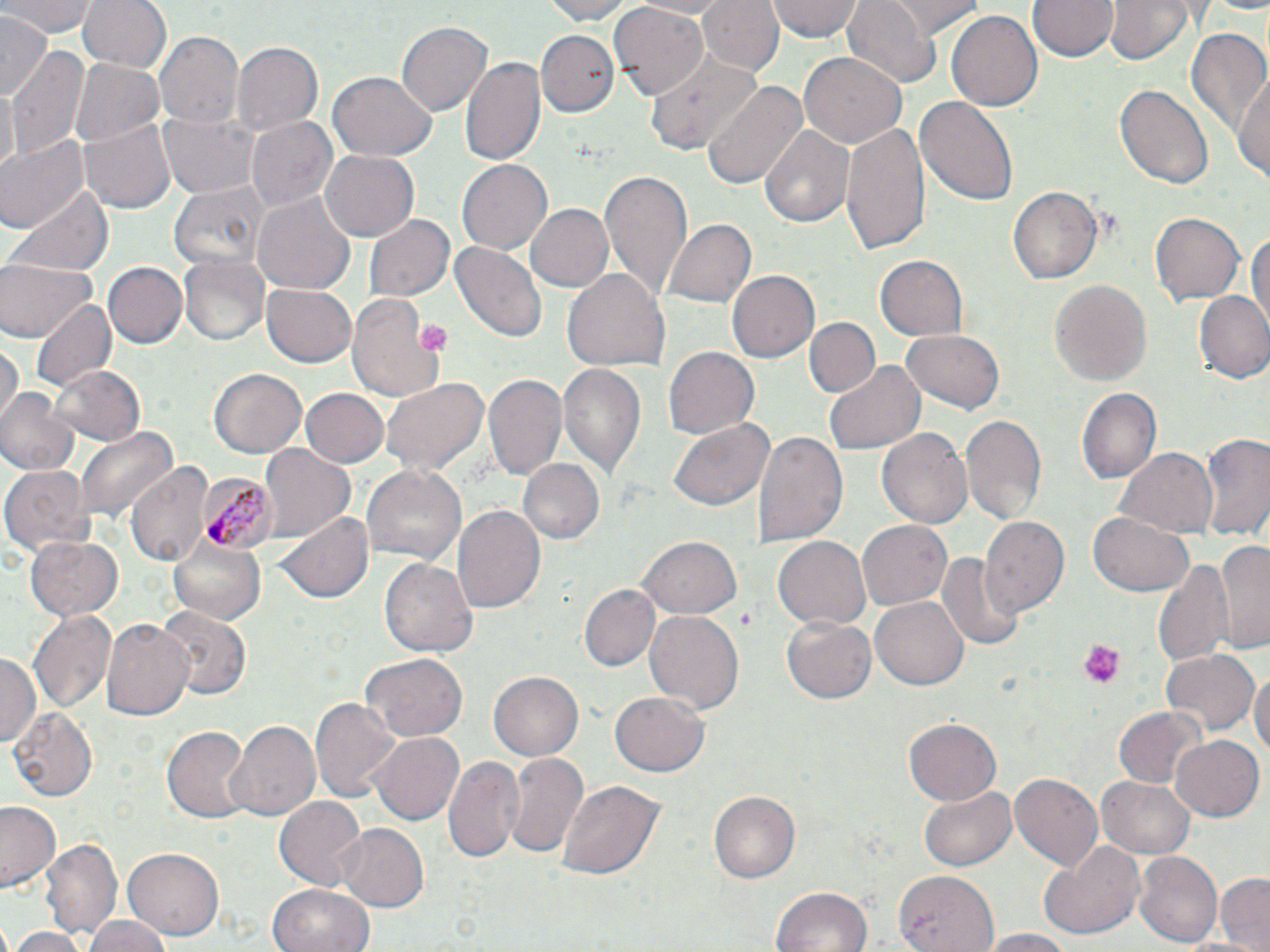 Approximate bounding boxes as [x1, y1, x2, y2] in pixels. Uninfected red blood cell locations: [4, 0, 97, 36], [77, 0, 172, 75], [537, 0, 635, 23], [695, 0, 783, 77], [767, 0, 863, 42], [843, 0, 943, 90], [889, 0, 983, 36], [1028, 0, 1116, 62], [1104, 0, 1201, 66], [609, 3, 708, 100], [945, 9, 1042, 113], [0, 11, 50, 102], [533, 18, 688, 109], [396, 20, 493, 115], [1184, 26, 1269, 139], [536, 30, 618, 117], [155, 31, 243, 127], [231, 41, 322, 137], [9, 47, 87, 162], [645, 51, 761, 153], [799, 51, 908, 150], [461, 56, 547, 167], [72, 58, 166, 147], [327, 73, 438, 161], [1234, 76, 1269, 186], [701, 78, 806, 193], [1117, 83, 1212, 190], [914, 94, 1020, 206], [161, 110, 261, 199], [79, 116, 177, 214], [246, 117, 339, 214], [839, 121, 930, 257], [761, 126, 853, 227], [0, 134, 88, 240], [321, 148, 420, 241], [457, 161, 552, 254], [599, 170, 692, 300], [171, 179, 268, 270], [11, 182, 114, 276], [1007, 185, 1102, 285], [252, 192, 355, 295], [525, 203, 615, 293], [1151, 211, 1245, 306], [365, 212, 454, 302], [662, 218, 754, 309], [1246, 224, 1270, 343], [451, 241, 546, 343], [181, 255, 268, 345], [874, 255, 969, 343], [0, 260, 98, 341], [104, 262, 187, 350], [562, 268, 670, 374], [725, 269, 818, 363], [1048, 278, 1150, 386], [261, 283, 358, 367], [1194, 291, 1270, 383], [346, 295, 447, 400], [30, 296, 116, 396], [805, 317, 880, 398], [899, 330, 1006, 412], [1, 339, 21, 427], [662, 347, 758, 441], [558, 361, 649, 481], [824, 362, 925, 456], [50, 363, 147, 447], [210, 368, 307, 459], [485, 373, 567, 478], [379, 377, 488, 480], [300, 388, 388, 469], [1, 389, 79, 474], [1076, 389, 1160, 485], [961, 415, 1046, 528], [670, 419, 774, 511], [76, 426, 179, 523], [877, 427, 974, 529], [754, 428, 848, 550], [1196, 433, 1270, 544], [258, 443, 356, 541], [1115, 445, 1217, 537], [518, 458, 605, 545], [127, 461, 214, 571], [2, 464, 92, 557], [361, 464, 467, 569], [452, 505, 545, 614], [277, 511, 373, 604], [1088, 513, 1195, 597], [979, 516, 1069, 619], [857, 518, 953, 610], [25, 534, 122, 623], [642, 536, 741, 617], [772, 536, 872, 632], [169, 537, 264, 625], [1216, 539, 1270, 653], [935, 548, 1024, 654], [381, 558, 478, 659], [1149, 559, 1238, 668], [581, 584, 661, 672], [872, 596, 973, 689], [157, 607, 249, 700], [642, 609, 744, 716], [27, 610, 117, 717], [782, 616, 876, 704], [103, 619, 193, 723], [1160, 648, 1259, 738], [361, 652, 468, 743], [0, 653, 41, 749], [1250, 667, 1270, 761], [490, 672, 583, 759], [611, 689, 709, 776], [311, 693, 403, 803], [10, 707, 99, 801], [1113, 708, 1204, 788], [902, 717, 1002, 806], [228, 719, 321, 822], [162, 726, 250, 820], [371, 731, 464, 823], [1169, 735, 1263, 821], [502, 750, 591, 863], [442, 752, 525, 864], [1010, 773, 1102, 870], [553, 776, 667, 886], [1096, 776, 1195, 859], [919, 785, 1017, 871], [707, 790, 800, 885], [273, 794, 367, 891], [0, 801, 62, 892], [335, 823, 431, 913], [44, 834, 121, 945], [1039, 842, 1145, 941], [125, 846, 226, 939], [1136, 852, 1222, 948], [895, 868, 998, 950], [1215, 873, 1270, 951], [266, 883, 375, 952], [770, 887, 872, 952], [85, 916, 169, 951], [9, 926, 85, 952], [979, 929, 1076, 952]. Plasmodium malariae-infected red blood cell locations: [199, 472, 278, 558]. Platelet locations: [414, 318, 451, 357], [1077, 638, 1127, 687]. Slide-level diagnosis: Plasmodium malariae. 1000x magnification. Optical microscopy. Thin blood smear. May-Grünwald-Giemsa-stained preparation. One field of a larger specimen. Image is 1270×952 pixels.